Report the malaria status of this cell.
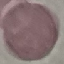

Uninfected.

Summary:
  - Preparation: thin smear
  - Capture: smartphone camera at the microscope eyepiece
  - Stain: Giemsa
  - Image type: cell patch, automatically extracted from a larger field of view and resized to 64 × 64 pixels